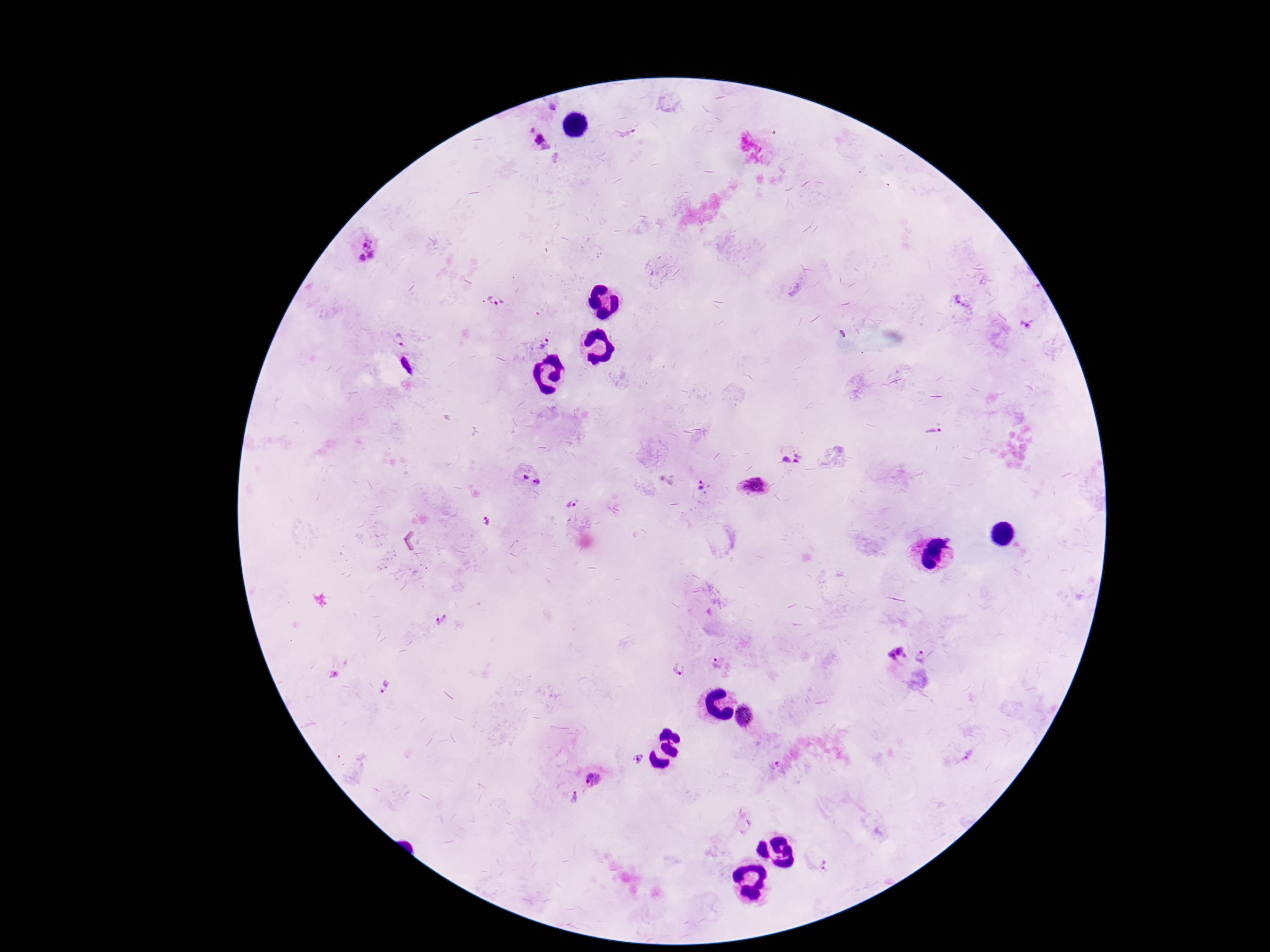 Approximate centers as {x, y} in pixels. Plasmodium parasite locations: {553, 108}, {532, 130}, {628, 135}, {539, 138}, {368, 243}, {371, 256}, {361, 258}, {489, 297}, {958, 299}, {502, 301}, {495, 303}, {1027, 325}, {398, 339}, {547, 340}, {542, 346}, {933, 431}, {798, 458}, {786, 460}, {527, 478}, {536, 482}, {700, 484}, {753, 487}, {572, 503}, {487, 521}, {440, 621}, {899, 650}, {893, 655}, {905, 655}, {920, 657}, {717, 664}, {678, 670}, {386, 687}, {744, 715}, {967, 757}, {638, 758}, {777, 763}, {593, 779}, {574, 798}, {825, 865}. One field from this slide. Patient malaria status: infected. Thick blood film. Image is 1270×952 pixels. Smartphone photograph taken through the microscope eyepiece. 100x magnification. Giemsa-stained preparation.